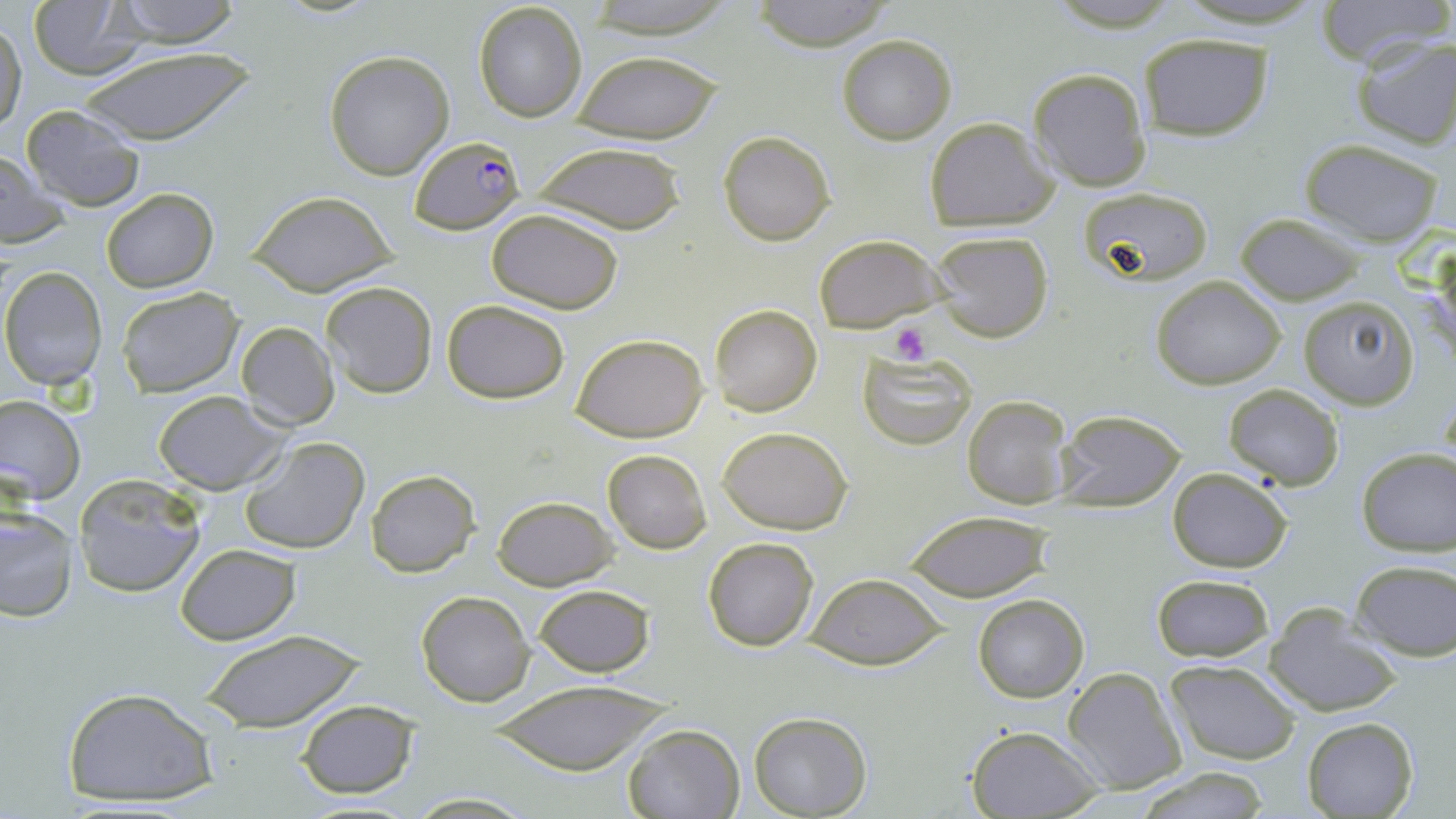

slide-level diagnosis = Plasmodium falciparum
platelet locations = approximate bounding boxes as [x1, y1, x2, y2] in pixels: [890, 322, 932, 364]
Plasmodium falciparum-infected red blood cell locations = approximate bounding boxes as [x1, y1, x2, y2] in pixels: [409, 135, 526, 234]
uninfected red blood cell locations = approximate bounding boxes as [x1, y1, x2, y2] in pixels: [105, 0, 246, 46], [574, 0, 739, 38], [748, 0, 897, 51], [1311, 0, 1452, 67], [473, 1, 588, 123], [27, 2, 146, 79], [1, 17, 26, 136], [1348, 31, 1456, 149], [1136, 33, 1275, 140], [837, 34, 957, 145], [74, 46, 259, 144], [571, 51, 722, 143], [324, 52, 454, 180], [1027, 68, 1151, 192], [18, 104, 146, 210], [924, 116, 1060, 228], [718, 131, 834, 245], [1299, 138, 1445, 246], [529, 142, 688, 234], [0, 150, 73, 250], [1081, 185, 1213, 285], [101, 187, 218, 294], [247, 189, 397, 295], [484, 208, 626, 312], [1235, 213, 1364, 306], [930, 231, 1054, 343], [814, 235, 942, 332], [1430, 243, 1456, 376], [1, 266, 108, 390], [1150, 276, 1285, 390], [321, 281, 437, 398], [116, 286, 242, 397], [1298, 295, 1417, 408], [441, 299, 572, 404], [711, 304, 822, 417], [236, 322, 341, 430], [570, 333, 710, 441], [857, 350, 977, 449], [1224, 384, 1344, 490], [154, 391, 286, 494], [1, 394, 85, 505], [962, 394, 1072, 510], [1054, 410, 1186, 511], [717, 426, 854, 535], [240, 435, 370, 557], [1356, 447, 1456, 555], [602, 449, 711, 554], [1166, 466, 1293, 573], [365, 470, 480, 576], [72, 475, 205, 599], [490, 495, 618, 590], [0, 504, 76, 623], [905, 512, 1049, 602], [702, 536, 820, 653], [176, 544, 300, 644], [1352, 559, 1456, 661], [804, 573, 949, 671], [1150, 573, 1274, 663], [533, 584, 655, 676], [416, 590, 534, 707], [972, 594, 1088, 703], [1267, 605, 1399, 717], [200, 629, 365, 733], [1165, 660, 1301, 766], [1063, 667, 1188, 793], [486, 680, 674, 775], [59, 685, 222, 811], [295, 699, 419, 797], [749, 711, 871, 817], [1301, 716, 1418, 818], [622, 723, 744, 818], [965, 726, 1104, 818], [1134, 767, 1272, 819], [402, 792, 537, 818]
field of view = one of a larger specimen
magnification = 1000x
preparation = thin blood smear
image size = 1456×819 pixels
modality = light microscopy
stain = May-Grünwald-Giemsa